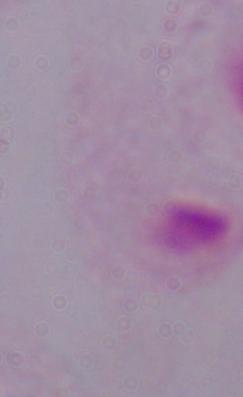

Summary:
  - Magnification: 1000x
  - Identification: trichomonad
  - Modality: micrograph